Locate every uninfected red blood cell.
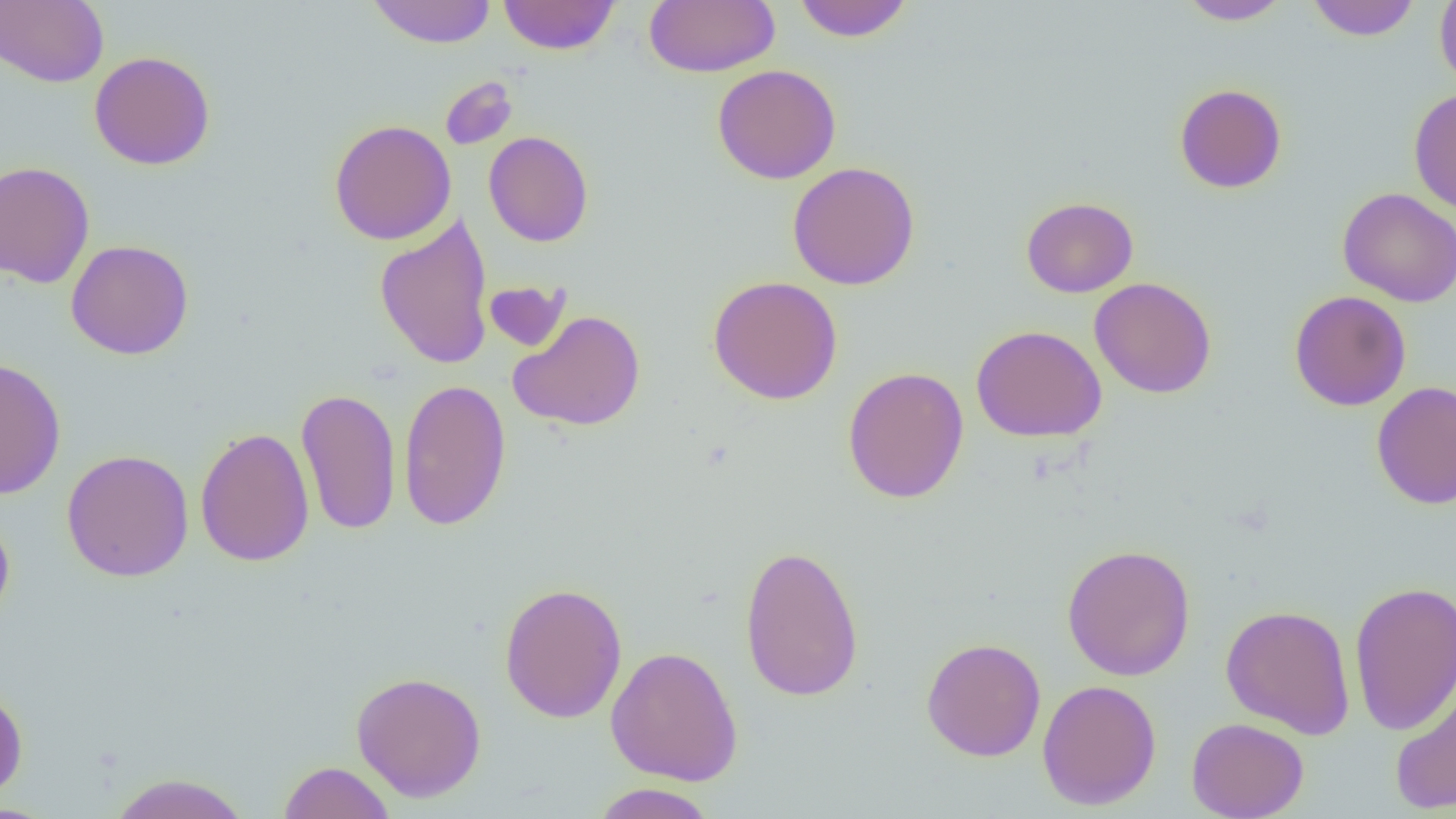
Approximate bounding boxes as (x1, y1, x2, y2) in pixels.
Uninfected red blood cells: (0, 0, 109, 88), (366, 0, 498, 48), (498, 0, 620, 55), (643, 0, 779, 77), (793, 0, 913, 43), (1177, 0, 1292, 25), (1305, 0, 1420, 41), (1434, 0, 1456, 90), (89, 50, 216, 171), (712, 64, 841, 185), (439, 76, 518, 150), (1174, 83, 1287, 194), (1408, 87, 1456, 215), (329, 119, 457, 245), (483, 131, 594, 247), (0, 160, 96, 288), (787, 161, 920, 290), (1337, 187, 1456, 307), (1021, 196, 1138, 298), (374, 213, 495, 370), (66, 239, 194, 360), (707, 275, 843, 405), (1089, 277, 1217, 399), (483, 280, 571, 352), (1289, 290, 1411, 411), (507, 309, 646, 431), (971, 324, 1107, 443), (0, 356, 67, 500), (842, 366, 969, 504), (397, 378, 512, 531), (1371, 381, 1456, 509), (296, 386, 401, 537), (194, 427, 315, 567), (61, 448, 194, 583), (0, 508, 15, 627), (740, 543, 865, 703), (1061, 544, 1196, 681), (1348, 580, 1455, 736), (499, 581, 628, 724), (1220, 604, 1356, 738), (921, 637, 1046, 762), (605, 645, 744, 786), (351, 670, 487, 802), (1389, 670, 1456, 816), (1037, 679, 1162, 810), (0, 684, 29, 802), (1186, 717, 1309, 819), (277, 760, 395, 819), (107, 772, 253, 818), (589, 783, 719, 819).

slide-level diagnosis = no evidence of blood parasites
preparation = thin blood smear
magnification = 1000x
modality = optical microscopy
image size = 1456×819 pixels
field of view = one of a larger specimen